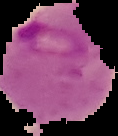 The area outside the segmented cell region is set to black. From a thin blood film. Image is 118×136 pixels. Malaria status: parasitized.